Locate every blood parasite and identify its species.
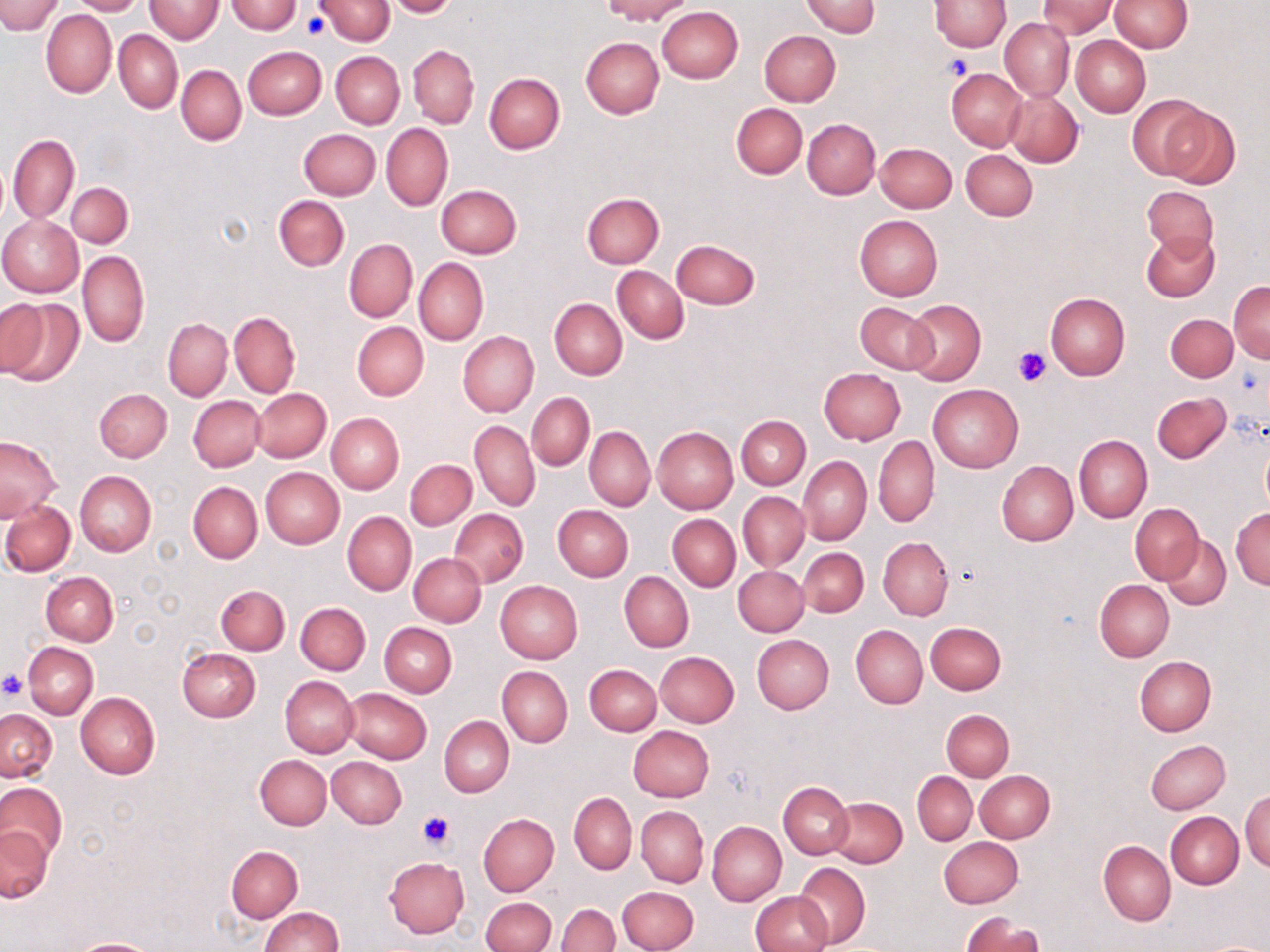
No blood parasites observed.

Summary:
  - Coordinate format: approximate bounding boxes as [x1, y1, x2, y2] in pixels
  - Platelet locations: [301, 14, 327, 41], [943, 54, 972, 81], [1013, 346, 1053, 388], [0, 671, 29, 700], [418, 810, 457, 852]
  - Uninfected red blood cell locations: [0, 0, 65, 35], [68, 0, 144, 15], [145, 0, 223, 43], [316, 0, 394, 45], [384, 0, 459, 18], [601, 0, 692, 23], [800, 0, 879, 38], [930, 0, 1011, 50], [1038, 0, 1115, 39], [1108, 0, 1192, 52], [227, 1, 302, 33], [657, 6, 743, 83], [41, 9, 115, 98], [999, 18, 1074, 101], [114, 29, 182, 112], [759, 30, 840, 106], [1071, 36, 1151, 117], [581, 37, 665, 117], [409, 44, 479, 128], [242, 47, 326, 119], [330, 52, 405, 128], [176, 65, 246, 145], [947, 69, 1027, 150], [484, 73, 565, 154], [1004, 91, 1084, 167], [1128, 94, 1213, 178], [731, 103, 807, 179], [1160, 105, 1239, 190], [803, 119, 880, 198], [381, 124, 453, 211], [298, 128, 380, 200], [9, 134, 79, 224], [875, 143, 956, 213], [961, 148, 1037, 220], [66, 183, 132, 248], [436, 185, 521, 258], [1142, 185, 1219, 257], [582, 193, 664, 268], [274, 196, 349, 271], [0, 215, 84, 297], [854, 215, 943, 300], [1141, 230, 1219, 303], [344, 239, 417, 322], [671, 240, 761, 309], [77, 251, 149, 348], [414, 257, 488, 346], [612, 266, 688, 344], [1228, 281, 1269, 363], [1045, 292, 1130, 380], [0, 298, 85, 390], [550, 299, 627, 379], [903, 300, 985, 385], [855, 302, 937, 374], [229, 311, 300, 397], [1166, 313, 1238, 381], [163, 319, 232, 400], [352, 321, 429, 401], [457, 330, 539, 417], [818, 367, 906, 445], [927, 384, 1024, 473], [94, 387, 172, 462], [252, 388, 332, 462], [1152, 391, 1232, 464], [527, 393, 594, 470], [189, 395, 265, 471], [326, 413, 403, 494], [736, 415, 810, 490], [469, 419, 540, 512], [585, 427, 654, 511], [652, 427, 738, 514], [1074, 434, 1152, 523], [0, 435, 61, 524], [873, 435, 939, 527], [1260, 441, 1270, 516], [798, 456, 871, 544], [406, 459, 476, 531], [996, 460, 1077, 546], [261, 467, 344, 547], [74, 470, 156, 557], [189, 482, 262, 563], [738, 492, 809, 570], [1, 499, 76, 577], [1131, 503, 1204, 584], [552, 505, 632, 582], [1231, 506, 1270, 590], [450, 509, 527, 587], [343, 512, 416, 595], [667, 513, 740, 591], [1162, 535, 1231, 611], [878, 536, 952, 620], [798, 548, 868, 618], [409, 553, 486, 627], [734, 565, 808, 636], [619, 571, 694, 652], [41, 572, 118, 646], [1095, 580, 1174, 662], [495, 581, 583, 664], [216, 584, 289, 655], [295, 603, 370, 675], [378, 622, 457, 697], [925, 622, 1006, 694], [850, 624, 926, 708], [752, 634, 834, 715], [23, 642, 98, 718], [177, 649, 260, 722], [655, 651, 739, 728], [1135, 656, 1216, 735], [585, 663, 661, 735], [497, 666, 572, 747], [281, 676, 358, 758], [343, 688, 432, 763], [75, 692, 160, 779], [0, 709, 56, 781], [941, 709, 1013, 781], [440, 716, 514, 797], [628, 726, 714, 803], [1146, 739, 1230, 814], [255, 754, 331, 829], [328, 756, 407, 827], [975, 770, 1054, 843], [912, 771, 977, 845], [778, 782, 854, 859], [0, 784, 66, 867], [1241, 789, 1269, 872], [568, 793, 637, 874], [827, 796, 908, 867], [637, 806, 708, 887], [1165, 812, 1243, 888], [479, 814, 558, 895], [707, 820, 786, 907], [1, 825, 53, 903], [939, 836, 1023, 908], [1099, 841, 1175, 925], [226, 845, 302, 922], [383, 857, 469, 938], [795, 862, 870, 948], [616, 885, 699, 952], [750, 892, 832, 952], [481, 898, 555, 952], [556, 903, 620, 952], [258, 907, 343, 952], [961, 912, 1045, 952], [69, 938, 163, 952], [1199, 940, 1269, 952]
  - Slide-level diagnosis: no evidence of blood parasites
  - Magnification: 1000x
  - Modality: optical microscopy
  - Field of view: single
  - Preparation: thin blood smear
  - Image size: 1270×952 pixels
  - Stain: May-Grünwald-Giemsa